Mark where platelets are.
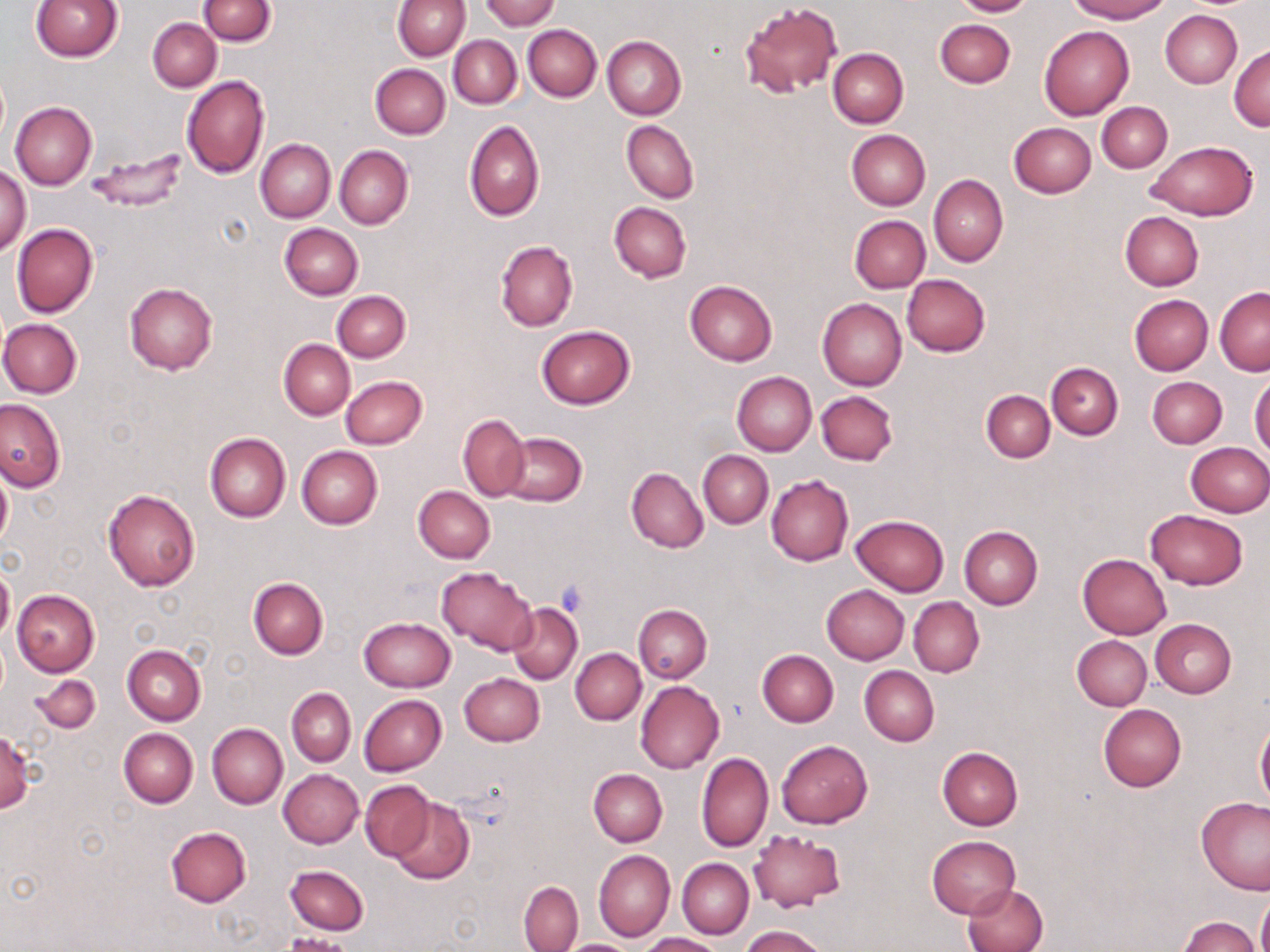
Approximate bounding boxes as [x1, y1, x2, y2] in pixels.
Platelets: [557, 579, 591, 616].

Summary:
  - Uninfected red blood cell locations: [31, 0, 124, 62], [199, 0, 276, 47], [392, 0, 471, 60], [481, 0, 559, 30], [950, 0, 1034, 17], [1067, 0, 1171, 22], [740, 1, 842, 98], [1160, 10, 1242, 89], [148, 18, 221, 91], [934, 19, 1015, 88], [522, 24, 601, 102], [1039, 25, 1134, 120], [449, 35, 521, 109], [602, 36, 686, 120], [1229, 44, 1270, 131], [828, 48, 908, 127], [370, 64, 450, 139], [182, 75, 270, 179], [9, 101, 97, 190], [1097, 102, 1172, 173], [464, 120, 545, 222], [621, 121, 699, 204], [1008, 122, 1096, 199], [846, 130, 930, 210], [255, 138, 336, 222], [1143, 141, 1258, 220], [335, 146, 414, 229], [86, 148, 188, 213], [0, 166, 31, 255], [928, 175, 1008, 267], [609, 202, 690, 282], [1120, 211, 1203, 290], [850, 216, 930, 292], [11, 223, 99, 319], [280, 223, 363, 300], [495, 241, 577, 332], [902, 273, 991, 356], [685, 279, 778, 366], [125, 283, 217, 375], [1216, 286, 1270, 376], [331, 290, 411, 362], [1130, 295, 1213, 376], [817, 298, 907, 391], [0, 318, 83, 398], [537, 325, 635, 409], [278, 338, 354, 420], [1047, 362, 1122, 439], [732, 371, 816, 457], [341, 376, 426, 449], [1148, 376, 1226, 447], [1250, 376, 1270, 459], [981, 389, 1054, 463], [816, 390, 898, 466], [0, 400, 64, 491], [458, 414, 530, 501], [205, 432, 291, 522], [501, 432, 587, 506], [1184, 443, 1270, 517], [296, 445, 383, 530], [698, 450, 773, 528], [0, 465, 12, 551], [626, 467, 708, 553], [766, 474, 854, 565], [413, 486, 495, 564], [103, 489, 200, 593], [1145, 509, 1248, 590], [850, 515, 949, 596], [959, 526, 1043, 609], [1076, 554, 1171, 639], [0, 564, 14, 642], [435, 565, 537, 656], [248, 577, 328, 659], [821, 585, 910, 664], [11, 589, 99, 677], [909, 597, 984, 678], [508, 602, 582, 685], [633, 604, 712, 683], [358, 617, 456, 692], [1151, 619, 1237, 698], [1073, 635, 1152, 711], [122, 645, 205, 726], [573, 646, 711, 735], [570, 648, 645, 724], [758, 650, 838, 726], [859, 665, 939, 746], [459, 672, 544, 746], [32, 674, 100, 733], [635, 681, 725, 773], [286, 687, 356, 766], [359, 694, 447, 776], [1098, 704, 1186, 791], [1255, 722, 1269, 807], [207, 723, 288, 809], [119, 728, 198, 808], [0, 730, 36, 813], [775, 741, 872, 828], [936, 747, 1023, 830], [696, 752, 773, 852], [588, 768, 667, 847], [278, 769, 363, 848], [360, 780, 434, 861], [389, 797, 474, 883], [1196, 798, 1270, 895], [166, 827, 252, 907], [748, 827, 845, 916], [926, 835, 1020, 919], [593, 849, 675, 942], [677, 858, 753, 938], [285, 864, 369, 935], [519, 882, 582, 951], [962, 883, 1048, 951], [1257, 891, 1270, 952], [1178, 915, 1259, 952], [740, 925, 829, 952], [281, 933, 354, 952], [640, 933, 723, 952], [557, 939, 641, 951]
  - Slide-level diagnosis: no evidence of blood parasites
  - Preparation: thin blood film
  - Image size: 1270×952 pixels
  - Stain: May-Grünwald-Giemsa
  - Modality: optical microscopy
  - Magnification: 1000x
  - Field of view: one of a larger specimen